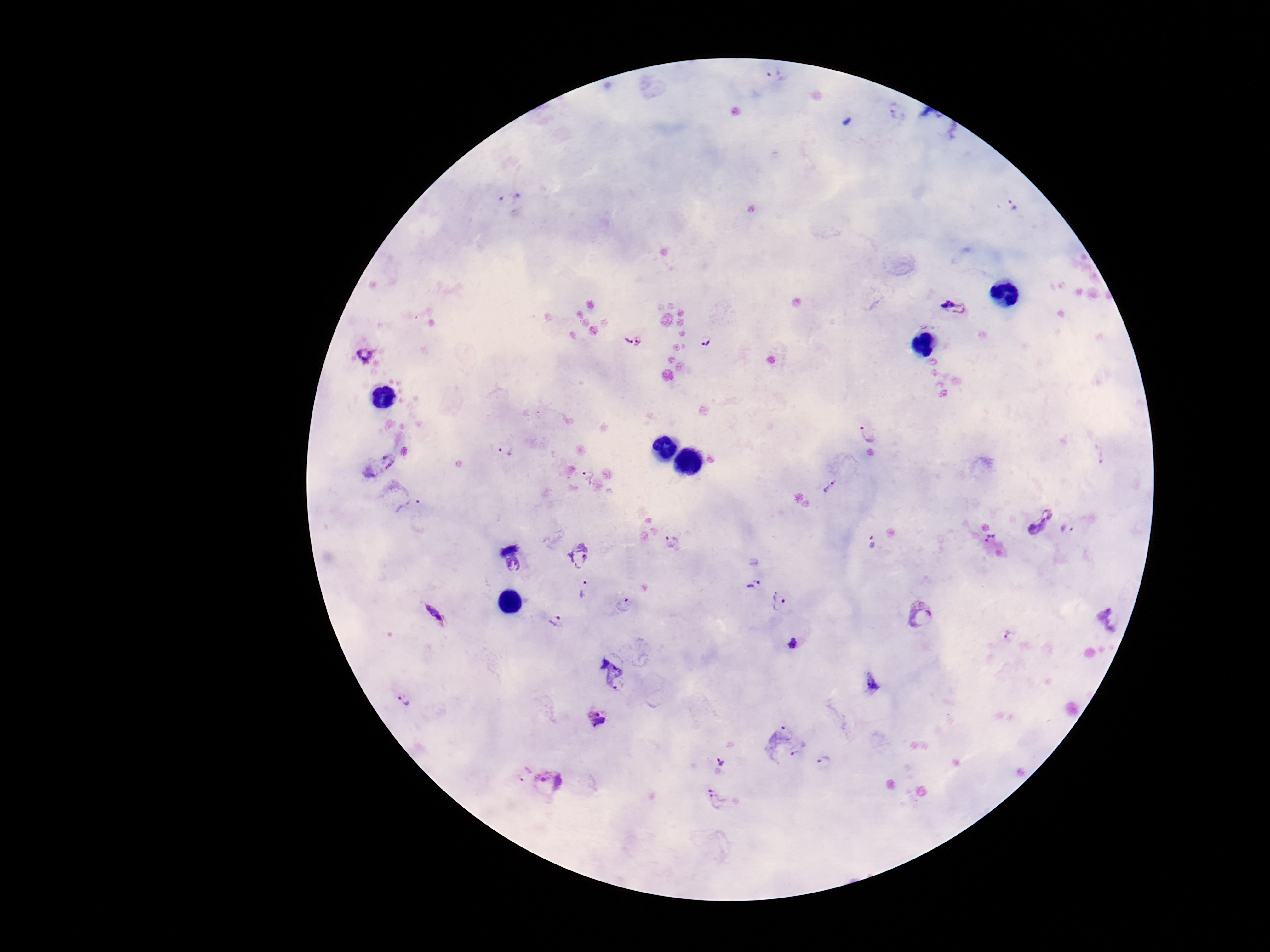
{
  "field_of_view": "one from this slide",
  "image_size": "1270×952 pixels",
  "patient_malaria_status": "infected",
  "magnification": "100x",
  "stain": "Giemsa",
  "plasmodium_parasite_locations": "approximate centers as (x, y) in pixels: (776, 75), (897, 112), (510, 196), (1012, 204), (954, 306), (706, 340), (625, 341), (640, 341), (367, 354), (867, 432), (505, 449), (1099, 453), (376, 463), (590, 477), (831, 486), (404, 498), (1040, 518), (1068, 529), (990, 538), (673, 542), (872, 542), (580, 555), (515, 566), (753, 582), (586, 590), (779, 600), (626, 604), (435, 614), (920, 615), (1113, 620), (558, 621), (1010, 636), (793, 644), (614, 672), (872, 684), (404, 699), (598, 717), (787, 743), (721, 763), (826, 763), (521, 770), (549, 780), (718, 799)",
  "capture": "smartphone camera through the microscope eyepiece",
  "preparation": "thick peripheral-blood smear"
}